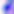
Summary:
  - Magnification: 400x
  - Identification: Toxoplasma gondii
  - Modality: micrograph